Identify the blood parasite species.
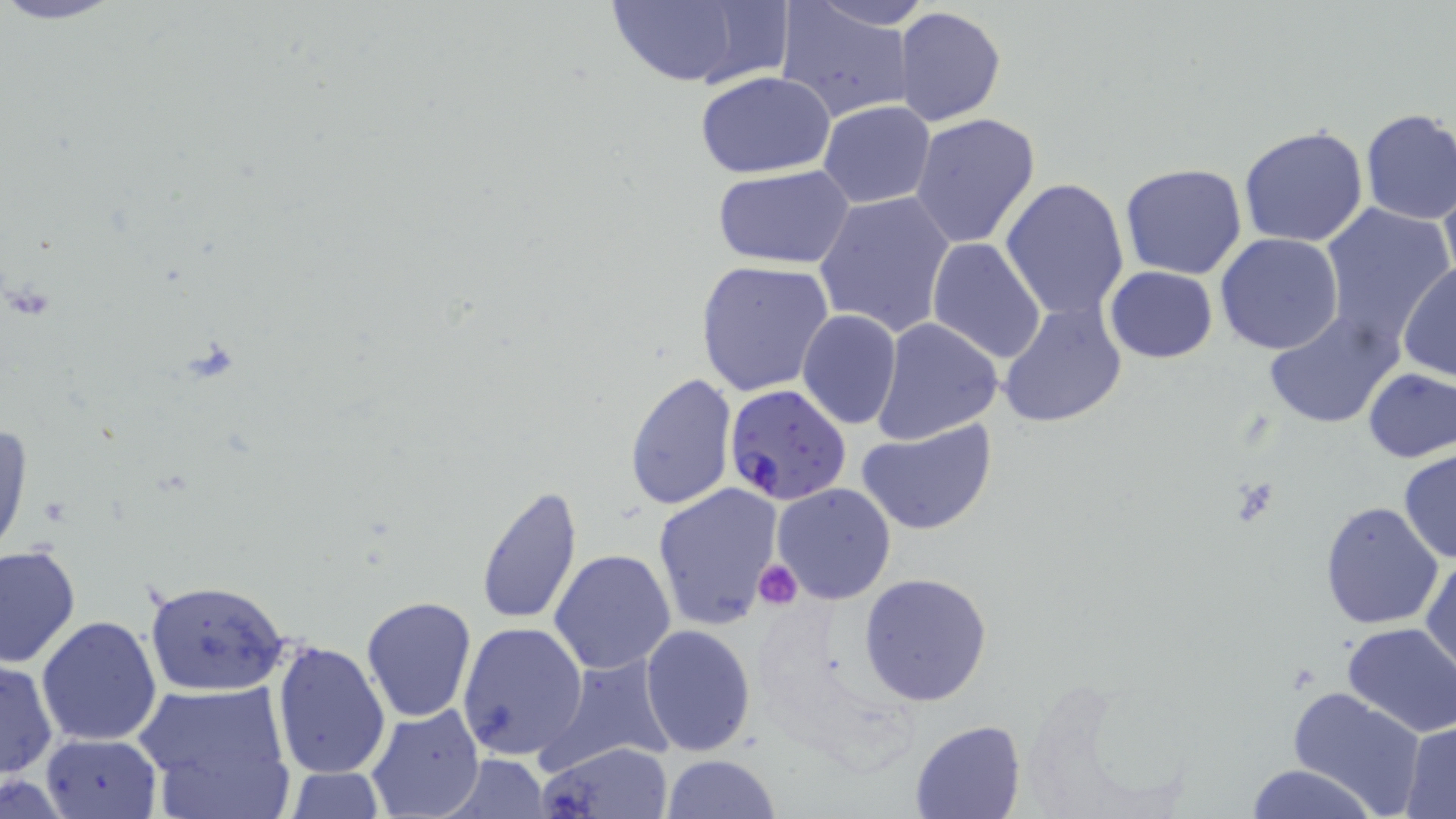

Plasmodium falciparum.

Summary:
  - Coordinate format: approximate bounding boxes as (x1,y1)-(x2,y2) corner pairs in pixels
  - Plasmodium falciparum-infected red blood cell locations: (723,382)-(852,506)
  - Uninfected red blood cell locations: (596,0)-(790,90), (808,1)-(932,30), (776,4)-(916,123), (894,6)-(1006,126), (695,71)-(840,179), (818,101)-(935,207), (1357,108)-(1456,225), (910,113)-(1042,252), (1238,124)-(1368,247), (1120,163)-(1248,280), (712,165)-(855,269), (1437,172)-(1456,296), (999,179)-(1130,320), (814,192)-(957,338), (1318,202)-(1453,347), (1215,233)-(1345,356), (928,237)-(1048,367), (695,260)-(837,399), (1397,263)-(1455,381), (1104,267)-(1219,362), (997,302)-(1127,427), (1263,310)-(1402,430), (796,311)-(903,430), (871,318)-(1002,443), (1361,367)-(1455,465), (624,372)-(737,510), (858,418)-(996,536), (0,419)-(31,562), (1397,448)-(1456,564), (653,483)-(785,633), (771,483)-(896,606), (474,484)-(583,626), (1318,501)-(1444,630), (0,544)-(81,669), (1421,546)-(1455,680), (549,549)-(676,675), (860,571)-(992,706), (143,576)-(296,698), (360,595)-(479,723), (36,614)-(164,746), (456,622)-(587,761), (1341,622)-(1456,738), (640,624)-(756,755), (271,639)-(392,780), (537,655)-(677,771), (1,660)-(59,779), (135,680)-(295,816), (1284,687)-(1427,817), (366,705)-(486,819), (908,719)-(1027,819), (1400,722)-(1456,817), (39,733)-(164,819), (538,739)-(671,819), (439,754)-(552,818), (661,754)-(782,817), (283,764)-(390,818), (1243,764)-(1380,819), (0,774)-(77,816)
  - Platelet locations: (753,561)-(802,611)
  - Field of view: one of a larger specimen
  - Image size: 1456×819 pixels
  - Magnification: 1000x
  - Modality: optical microscopy
  - Stain: May-Grünwald-Giemsa
  - Preparation: thin blood smear